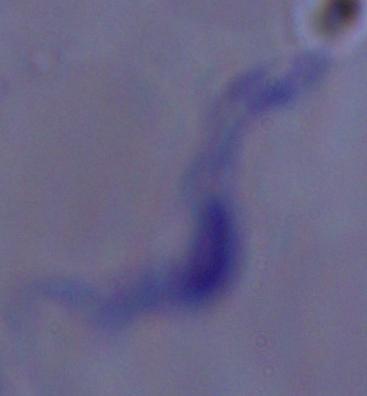

Summary:
  - Modality: micrograph
  - Magnification: 1000x
  - Identification: trypanosome